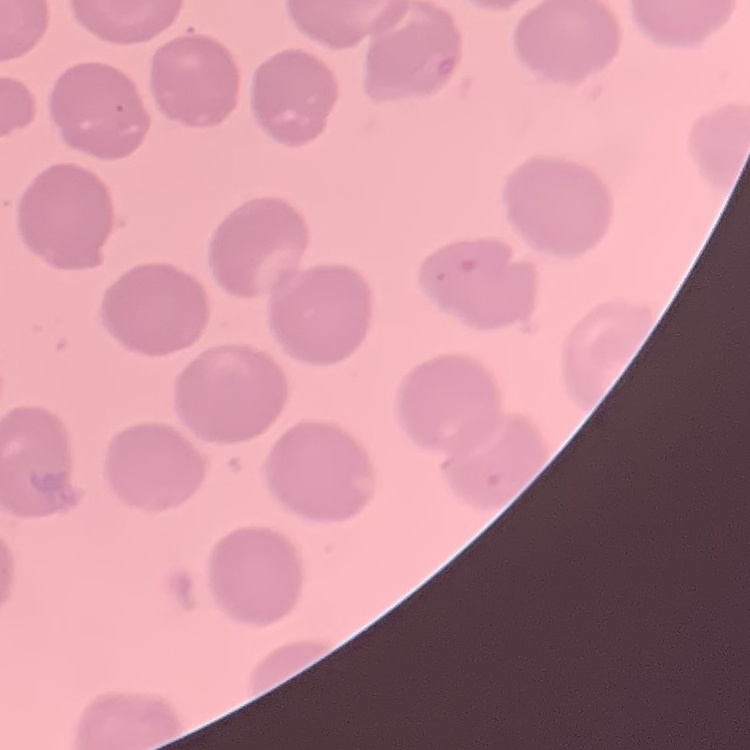
red blood cell morphology = no rouleaux formation
stain = Field's or Giemsa
image type = one tile cut from a larger photomicrograph
preparation = thin blood film